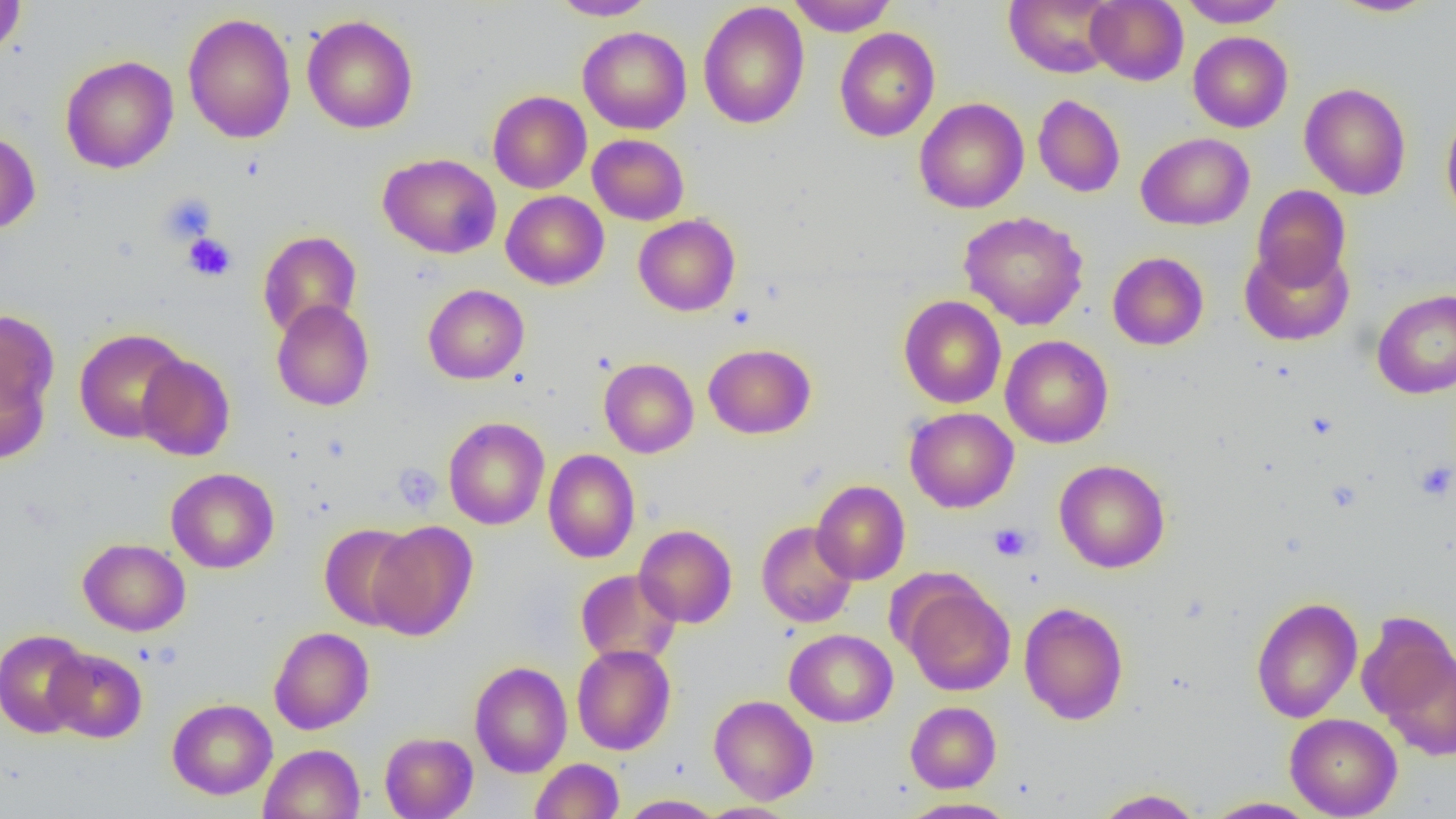
Summary:
  - Coordinate format: approximate bounding boxes as (x1,y1)-(x2,y2) corner pairs in pixels
  - Uninfected red blood cell locations: (550,0)-(658,20), (788,0)-(897,36), (1003,0)-(1119,78), (1086,0)-(1188,86), (1179,0)-(1289,28), (1329,0)-(1440,17), (0,1)-(27,56), (698,2)-(809,129), (183,12)-(296,144), (302,15)-(418,133), (578,27)-(692,134), (834,28)-(940,142), (1188,31)-(1293,133), (60,55)-(179,173), (1299,82)-(1412,199), (488,90)-(591,193), (1033,94)-(1126,198), (914,97)-(1029,213), (1441,107)-(1456,225), (0,130)-(40,235), (1136,132)-(1254,230), (588,134)-(689,225), (378,153)-(501,259), (1251,184)-(1351,289), (501,190)-(609,290), (958,211)-(1089,330), (633,214)-(740,316), (258,230)-(362,338), (1240,243)-(1355,346), (1108,252)-(1209,350), (423,284)-(529,384), (1372,288)-(1456,399), (898,295)-(1007,408), (272,299)-(374,411), (0,307)-(59,428), (73,328)-(191,443), (1000,335)-(1113,448), (703,343)-(816,439), (136,354)-(235,461), (599,358)-(699,458), (0,359)-(50,463), (905,407)-(1019,513), (443,417)-(550,530), (543,449)-(640,563), (1054,459)-(1170,573), (166,468)-(279,573), (811,480)-(910,585), (367,520)-(478,640), (756,521)-(858,628), (319,523)-(420,630), (634,524)-(737,628), (78,538)-(190,636), (576,569)-(681,666), (901,580)-(1015,696), (1250,596)-(1363,723), (1019,601)-(1129,725), (1360,615)-(1456,757), (269,626)-(374,734), (784,628)-(898,727), (0,629)-(92,738), (572,644)-(676,755), (45,648)-(147,743), (470,661)-(572,777), (709,694)-(818,805), (167,698)-(277,799), (905,701)-(1001,793), (1285,713)-(1402,818), (379,731)-(478,819), (259,744)-(364,819), (530,758)-(624,818), (1093,787)-(1204,818), (618,794)-(725,818), (1202,796)-(1321,818), (898,797)-(1018,818), (696,802)-(800,819)
  - Platelet locations: (159,192)-(217,245), (183,233)-(236,281), (1414,459)-(1456,501), (394,464)-(442,514), (989,523)-(1032,561)
  - Slide-level diagnosis: no evidence of blood parasites
  - Magnification: 1000x
  - Image size: 1456×819 pixels
  - Field of view: single
  - Modality: optical microscopy
  - Preparation: thin blood smear